Give the position of every leukocyte visible.
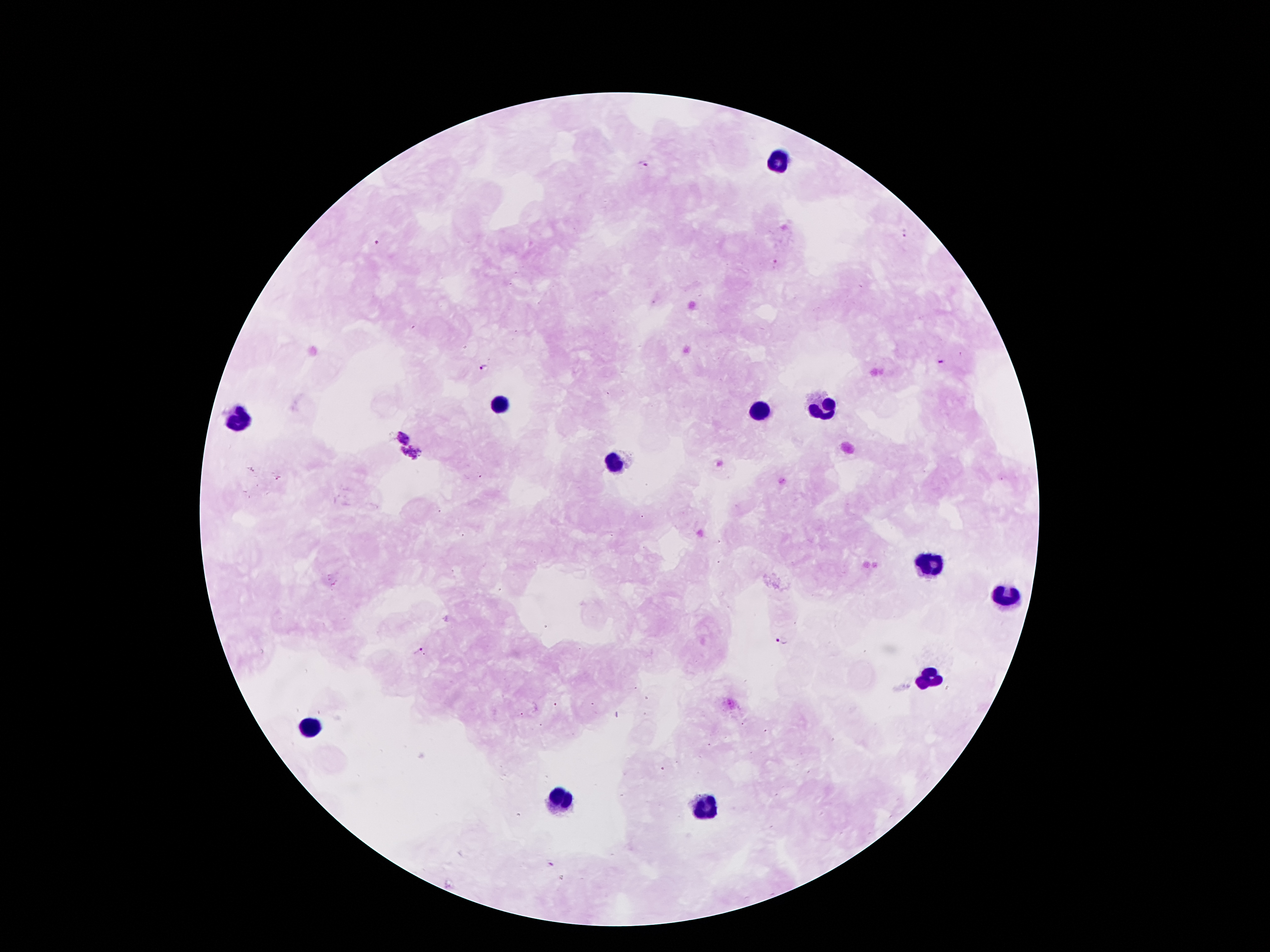

Approximate centers as {x, y} in pixels.
Leukocytes: {779, 161}, {501, 407}, {822, 407}, {761, 412}, {239, 418}, {615, 463}, {934, 560}, {1007, 598}, {929, 677}, {310, 726}, {562, 799}, {705, 810}.

Summary:
  - Plasmodium parasite locations: {642, 164}, {904, 231}, {375, 242}, {776, 262}, {939, 363}, {483, 368}, {400, 430}, {410, 457}, {277, 477}, {781, 641}, {418, 650}, {549, 864}
  - Image size: 1270×952 pixels
  - Stain: Giemsa
  - Preparation: thick blood film
  - Patient malaria status: positive for Plasmodium falciparum
  - Magnification: 100x
  - Field of view: one from this slide
  - Capture: smartphone through the microscope eyepiece